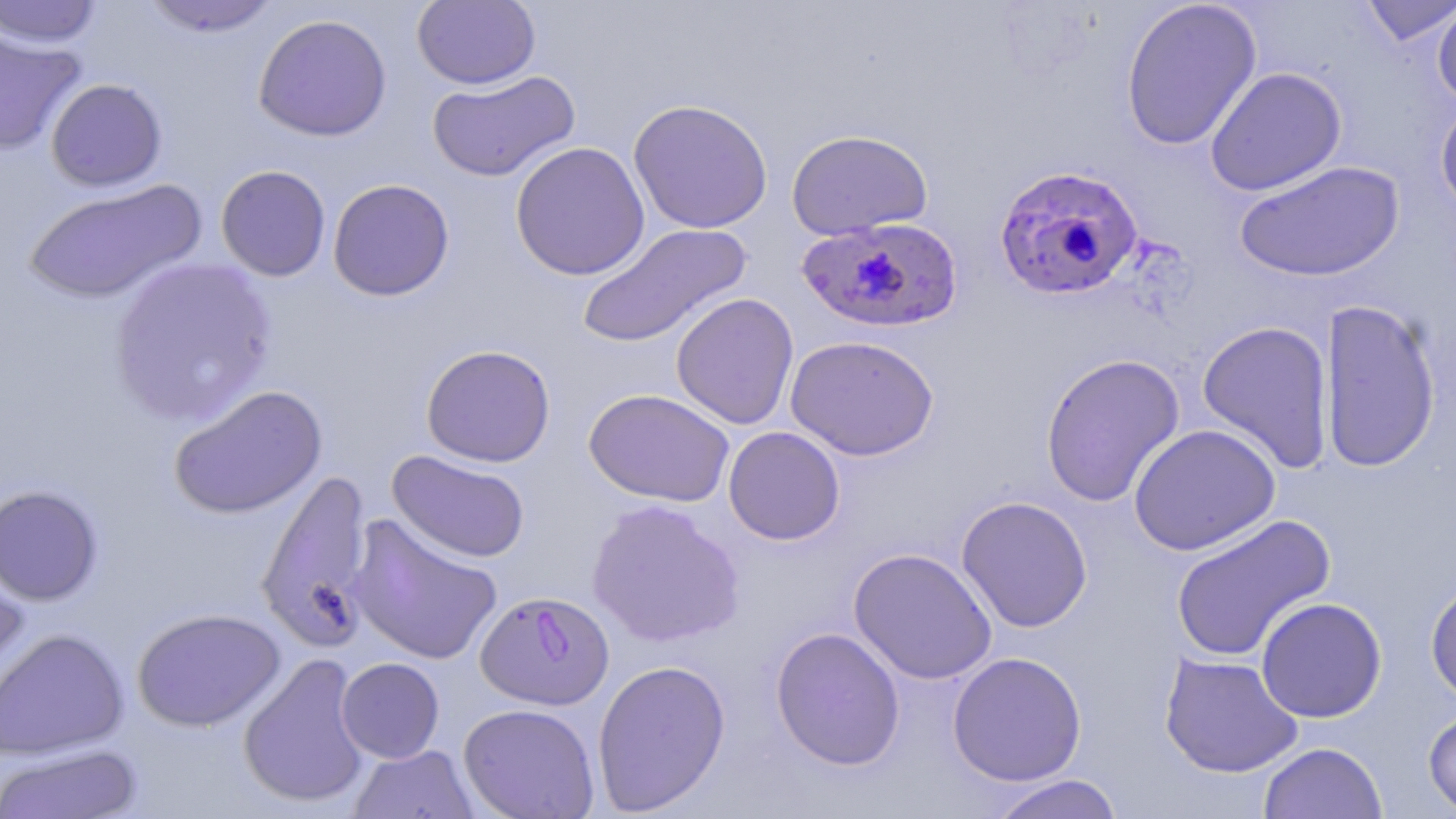

Approximate bounding boxes as [x1, y1, x2, y2] in pixels. Plasmodium falciparum-infected red blood cell locations: [994, 165, 1143, 302], [796, 217, 964, 334], [475, 590, 614, 710]. Uninfected red blood cell locations: [140, 0, 282, 37], [412, 0, 541, 90], [1119, 0, 1262, 151], [1359, 0, 1455, 47], [0, 1, 104, 48], [1432, 1, 1456, 109], [253, 13, 392, 142], [0, 27, 87, 155], [1204, 66, 1347, 196], [427, 70, 580, 182], [46, 78, 167, 191], [1435, 97, 1456, 219], [628, 98, 773, 234], [786, 129, 933, 241], [510, 141, 650, 281], [1234, 160, 1404, 282], [216, 164, 331, 281], [22, 178, 207, 305], [328, 178, 455, 301], [576, 222, 753, 349], [108, 257, 278, 427], [671, 292, 799, 430], [1318, 298, 1442, 474], [1196, 320, 1335, 474], [785, 334, 940, 461], [421, 344, 556, 468], [1040, 353, 1185, 508], [169, 384, 327, 519], [584, 388, 735, 507], [1128, 423, 1281, 556], [723, 426, 845, 545], [387, 450, 530, 563], [256, 468, 375, 651], [0, 483, 103, 606], [955, 495, 1093, 633], [586, 499, 745, 648], [347, 513, 503, 666], [1169, 514, 1336, 663], [848, 548, 997, 685], [0, 565, 31, 713], [1425, 576, 1456, 706], [1256, 597, 1387, 723], [132, 607, 285, 732], [770, 626, 906, 771], [0, 628, 129, 760], [947, 651, 1087, 786], [237, 652, 372, 809], [1159, 652, 1303, 778], [336, 657, 445, 763], [591, 659, 731, 815], [458, 703, 600, 819], [1422, 706, 1456, 816], [1258, 741, 1388, 819], [0, 743, 143, 818], [348, 744, 480, 819], [985, 774, 1126, 819]. Slide-level diagnosis: Plasmodium falciparum. Optical microscopy. May-Grünwald-Giemsa-stained preparation. Single field of view. Captured at 1000x magnification. Thin blood smear. Image is 1456×819 pixels.